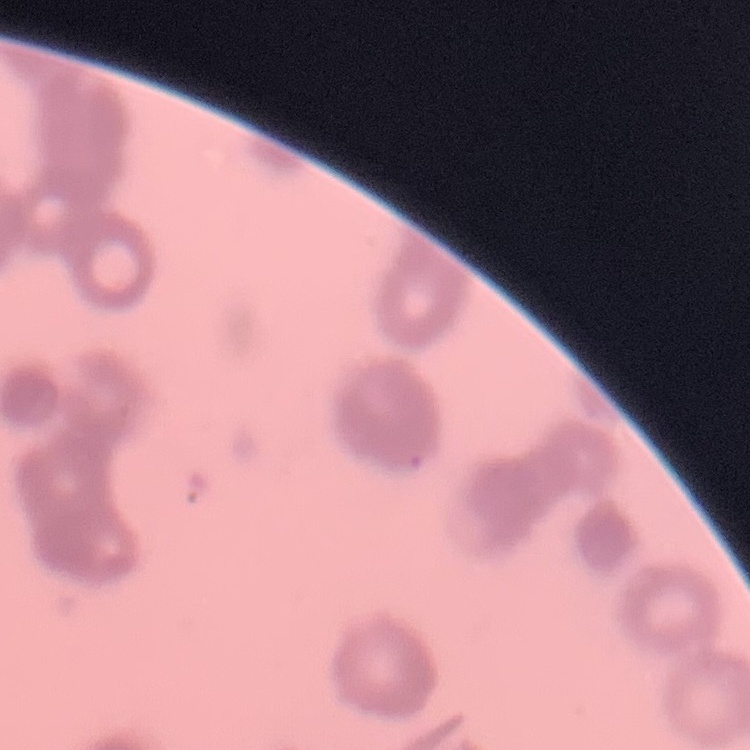 The erythrocytes show rouleaux formation. Square crop of a larger photomicrograph. Thin peripheral smear. Stained with either Field's or Giemsa.